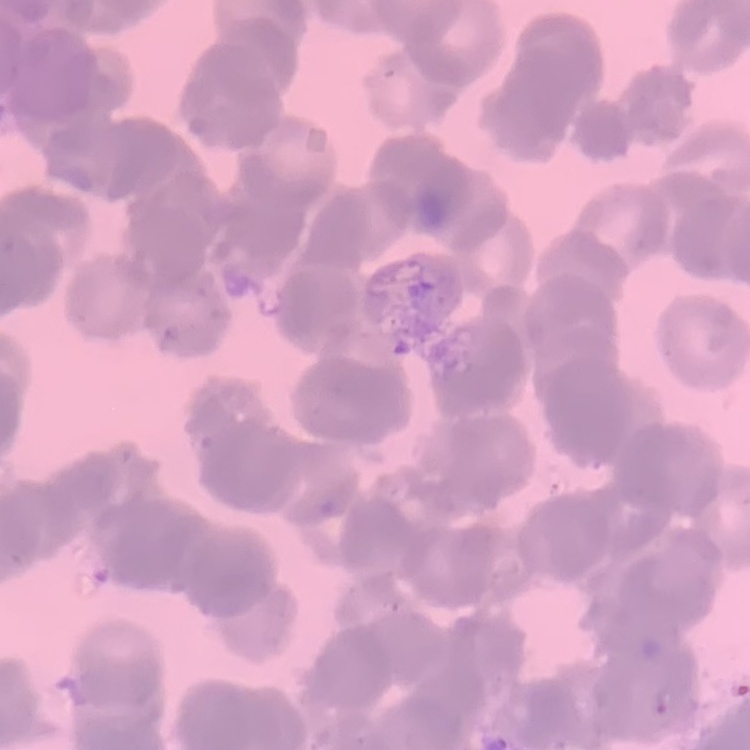
Summary:
  - Erythrocyte morphology: rouleaux formation
  - Stain: Field's or Giemsa
  - Preparation: thin blood smear
  - Image type: square crop of a larger photomicrograph